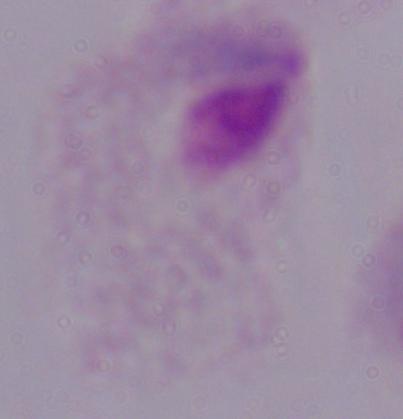
identification = trichomonad
magnification = 1000x
modality = micrograph